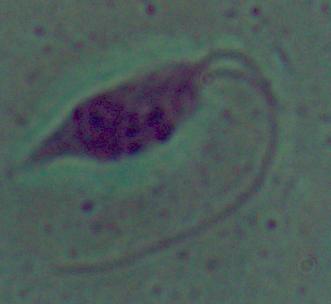

Photomicrograph. A Leishmania parasite is shown. Captured at 1000x magnification.